Outline each Plasmodium vivax-infected red blood cell.
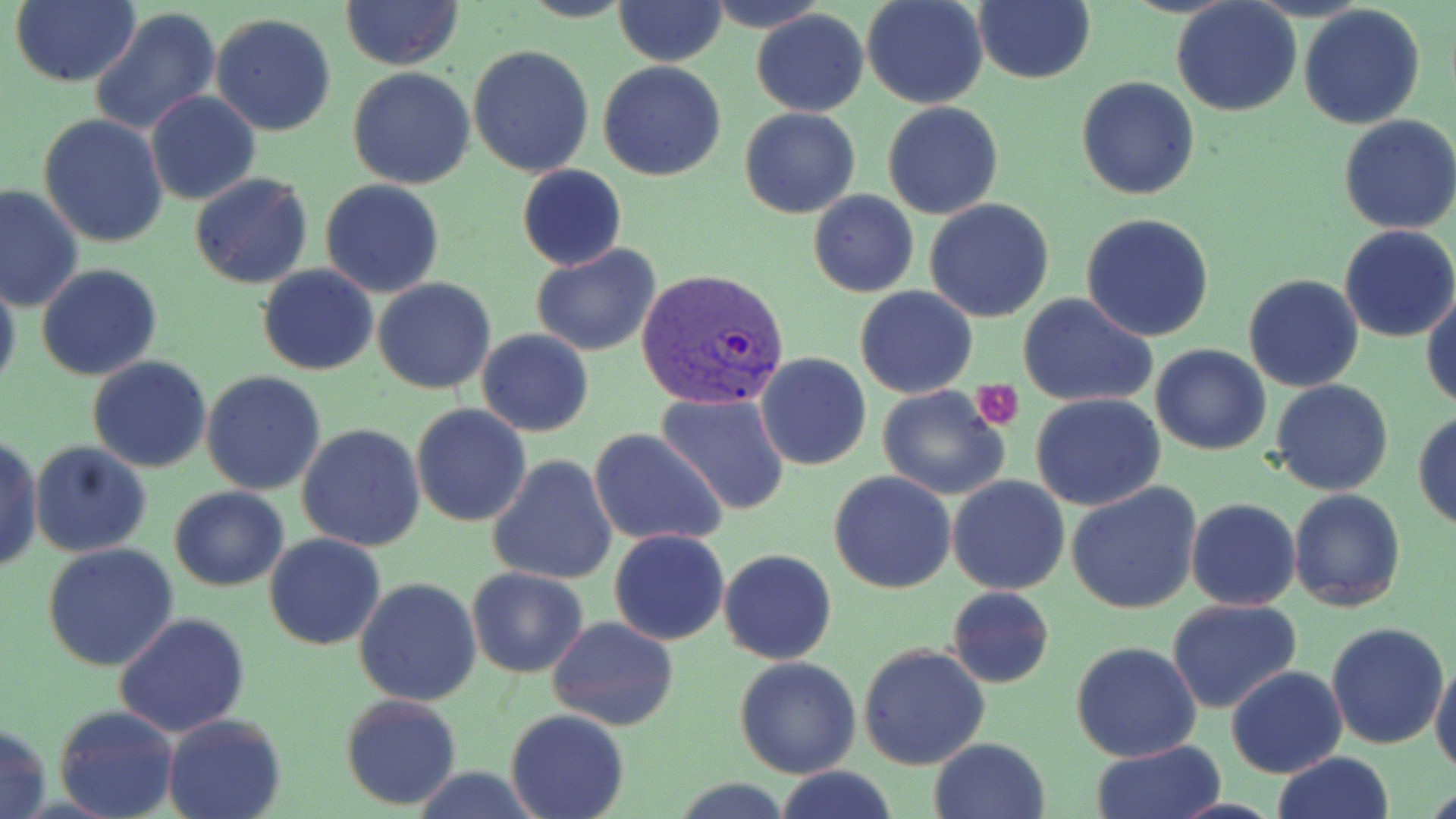
Approximate bounding boxes as [x1, y1, x2, y2] in pixels.
Plasmodium vivax-infected red blood cells: [636, 267, 792, 411].

slide-level diagnosis = Plasmodium vivax
preparation = thin blood film
modality = light microscopy
platelet locations = approximate bounding boxes as [x1, y1, x2, y2] in pixels: [971, 380, 1023, 430]
field of view = one of a larger specimen
image size = 1456×819 pixels
uninfected red blood cell locations = approximate bounding boxes as [x1, y1, x2, y2] in pixels: [11, 0, 142, 88], [340, 0, 463, 69], [612, 0, 727, 66], [705, 0, 828, 32], [862, 0, 988, 109], [973, 1, 1095, 85], [1170, 2, 1302, 117], [1298, 5, 1425, 130], [88, 7, 221, 138], [751, 9, 869, 116], [211, 13, 338, 136], [469, 43, 596, 178], [598, 62, 727, 183], [347, 67, 475, 189], [1077, 77, 1201, 201], [146, 91, 261, 206], [882, 101, 1004, 219], [739, 107, 860, 219], [38, 113, 169, 250], [1337, 114, 1456, 235], [517, 164, 626, 272], [188, 174, 312, 290], [320, 180, 445, 298], [1, 184, 85, 315], [808, 190, 920, 298], [925, 198, 1055, 321], [1082, 212, 1215, 342], [1337, 225, 1456, 344], [530, 243, 661, 358], [36, 264, 163, 382], [259, 265, 378, 376], [0, 272, 20, 399], [1244, 273, 1363, 392], [373, 276, 497, 394], [855, 286, 978, 399], [1421, 286, 1456, 411], [1016, 291, 1158, 409], [476, 328, 594, 437], [1150, 343, 1271, 455], [754, 353, 872, 473], [87, 357, 213, 472], [201, 372, 327, 495], [1269, 379, 1395, 497], [875, 383, 1013, 501], [657, 393, 790, 515], [1031, 393, 1167, 511], [411, 404, 531, 527], [1412, 410, 1456, 530], [296, 423, 426, 552], [590, 429, 729, 547], [0, 434, 43, 577], [30, 441, 152, 559], [487, 454, 618, 588], [829, 470, 957, 593], [948, 475, 1070, 594], [1066, 481, 1203, 615], [170, 487, 288, 590], [1288, 488, 1406, 611], [187, 499, 344, 616], [1187, 499, 1301, 610], [608, 529, 729, 646], [263, 533, 386, 651], [43, 543, 179, 671], [718, 549, 837, 664], [466, 566, 589, 678], [354, 576, 482, 706], [945, 586, 1055, 689], [1166, 598, 1302, 714], [115, 613, 250, 738], [546, 617, 678, 731], [1325, 623, 1450, 750], [1070, 641, 1202, 763], [858, 643, 991, 771], [733, 656, 861, 777], [1430, 659, 1456, 775], [1225, 666, 1347, 778], [340, 693, 463, 810], [54, 704, 178, 819], [506, 710, 631, 819], [163, 712, 287, 819], [0, 723, 50, 819], [929, 737, 1053, 819], [1091, 741, 1223, 819], [1271, 753, 1395, 819], [776, 767, 899, 819]
magnification = 1000x
stain = May-Grünwald-Giemsa